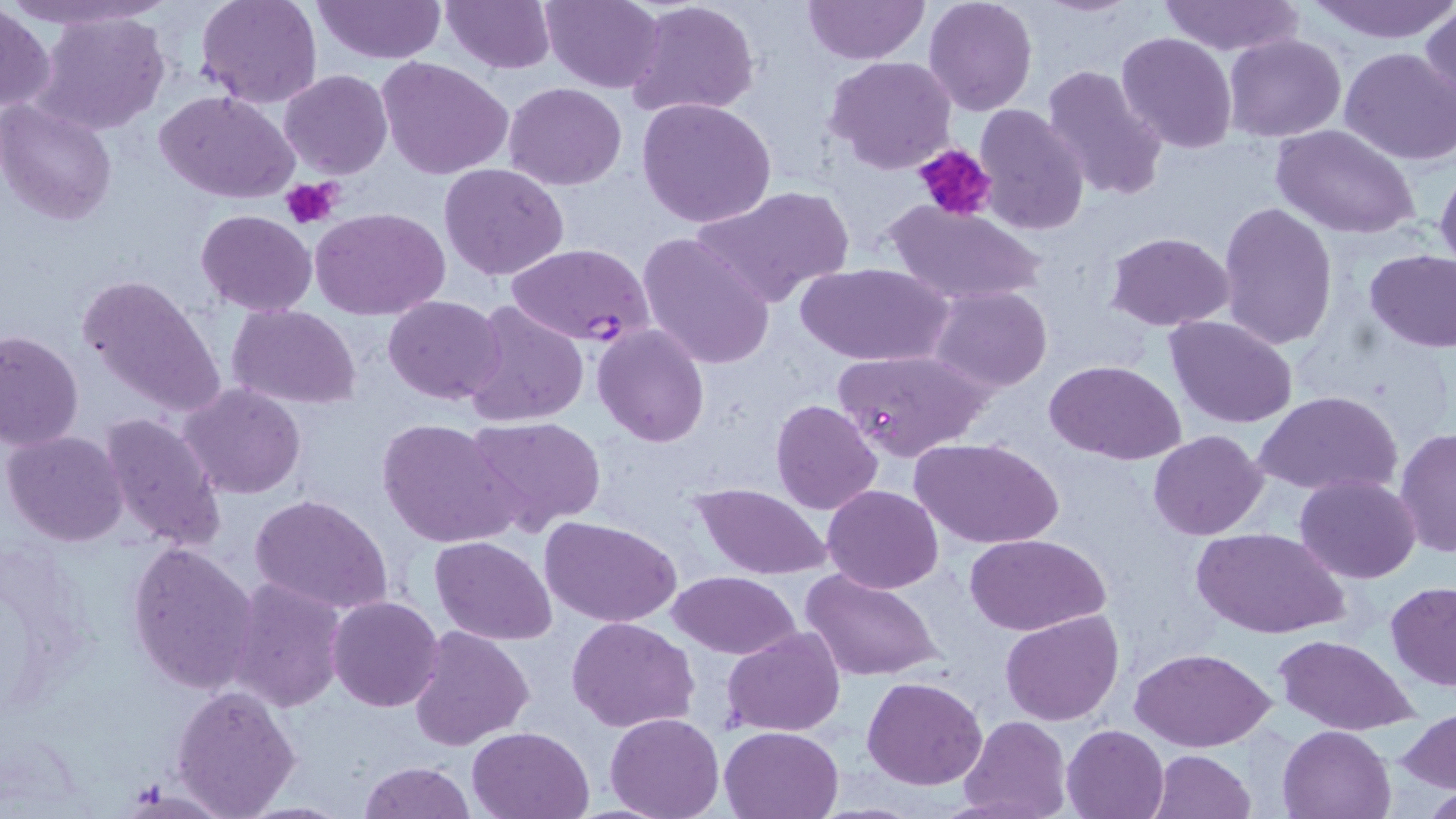

Summary:
  - Coordinate format: approximate bounding boxes as [x1, y1, x2, y2] in pixels
  - Uninfected red blood cell locations: [195, 0, 323, 109], [440, 0, 556, 73], [538, 0, 666, 92], [625, 0, 761, 121], [801, 0, 930, 66], [924, 0, 1037, 116], [1156, 0, 1301, 55], [1309, 0, 1456, 42], [311, 1, 446, 64], [0, 5, 53, 117], [1421, 5, 1455, 117], [31, 11, 169, 135], [1116, 32, 1236, 153], [1224, 33, 1346, 142], [1339, 46, 1455, 165], [826, 55, 958, 175], [377, 57, 513, 179], [1041, 63, 1166, 202], [281, 69, 392, 179], [504, 81, 626, 191], [157, 91, 299, 205], [637, 96, 776, 229], [1, 100, 119, 225], [972, 103, 1090, 235], [1272, 125, 1422, 239], [439, 163, 568, 281], [1435, 164, 1456, 276], [689, 185, 854, 306], [882, 199, 1049, 308], [1219, 199, 1338, 349], [310, 208, 449, 321], [197, 210, 316, 316], [1103, 230, 1236, 330], [637, 232, 776, 370], [1364, 251, 1456, 351], [794, 261, 953, 367], [76, 271, 227, 420], [928, 286, 1052, 393], [383, 295, 508, 404], [461, 301, 588, 427], [228, 304, 361, 409], [1165, 315, 1297, 428], [591, 323, 709, 447], [0, 329, 84, 450], [832, 347, 990, 461], [1047, 359, 1186, 464], [180, 384, 306, 499], [1254, 391, 1402, 498], [770, 399, 882, 514], [98, 411, 227, 553], [464, 414, 606, 534], [377, 417, 520, 548], [1395, 428, 1455, 557], [3, 430, 130, 547], [1149, 430, 1268, 541], [914, 437, 1063, 551], [1295, 473, 1419, 584], [691, 482, 834, 582], [823, 485, 944, 594], [249, 492, 394, 615], [540, 515, 682, 625], [1192, 527, 1348, 641], [967, 535, 1110, 636], [430, 536, 558, 645], [128, 541, 259, 696], [801, 565, 944, 683], [669, 571, 802, 658], [225, 579, 347, 712], [1385, 581, 1456, 691], [328, 595, 444, 712], [1001, 610, 1124, 727], [568, 616, 697, 733], [407, 625, 533, 752], [723, 627, 846, 737], [1274, 635, 1418, 735], [1130, 647, 1276, 751], [861, 677, 986, 790], [171, 683, 302, 816], [1399, 708, 1456, 795], [605, 711, 724, 819], [958, 715, 1070, 819], [1061, 723, 1168, 819], [1278, 723, 1395, 818], [468, 726, 593, 818], [720, 726, 843, 818], [1150, 750, 1256, 818], [358, 760, 474, 818]
  - Plasmodium falciparum-infected red blood cell locations: [504, 242, 658, 348]
  - Platelet locations: [912, 142, 998, 224], [281, 176, 343, 229]
  - Slide-level diagnosis: Plasmodium falciparum
  - Modality: optical microscopy
  - Preparation: thin blood film
  - Magnification: 1000x
  - Image size: 1456×819 pixels
  - Field of view: one of a larger specimen
  - Stain: May-Grünwald-Giemsa